Assess the morphology of the red blood cells.
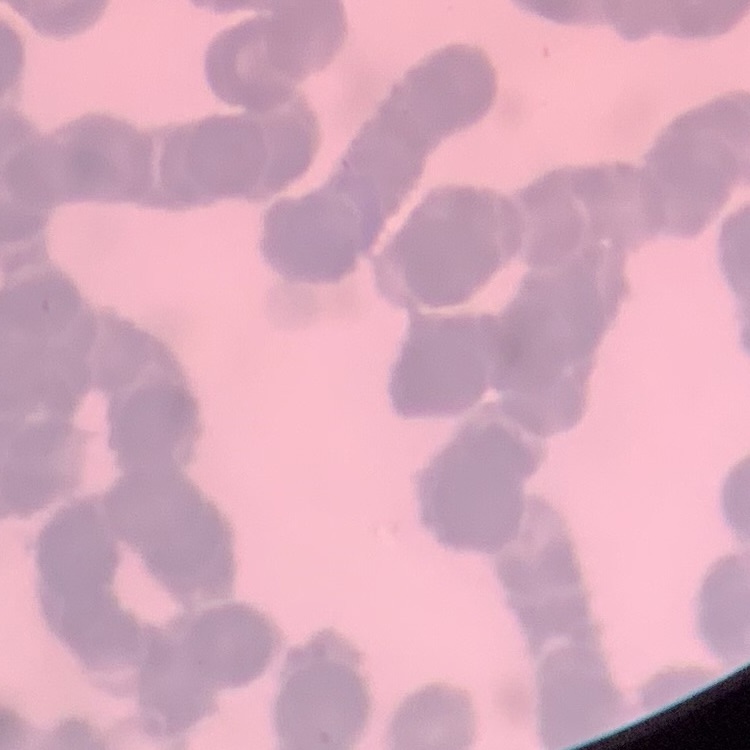
Rouleaux formation.

preparation: thin peripheral smear
stain: Field's or Giemsa
image_type: square crop of a larger photomicrograph